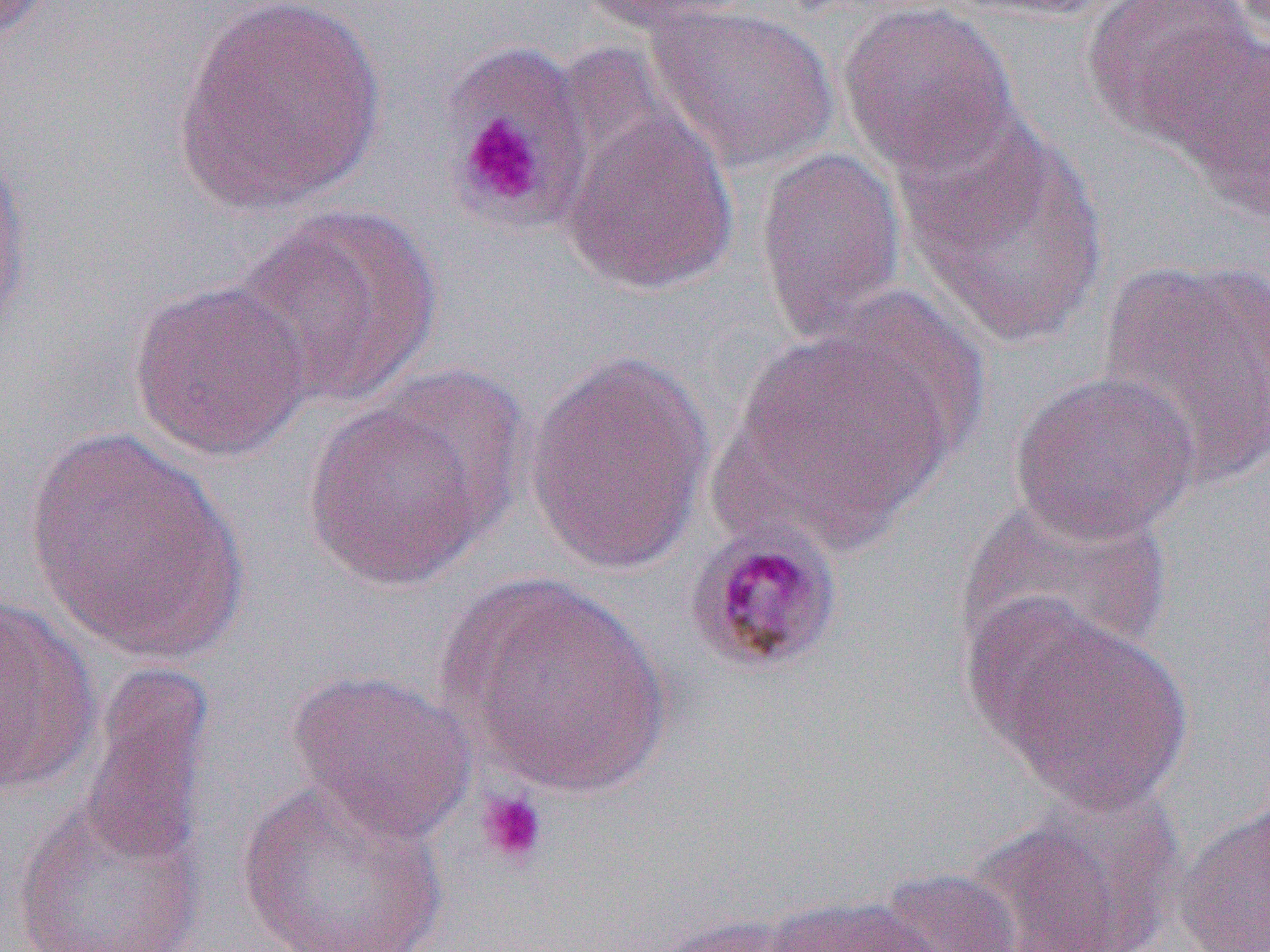
slide-level diagnosis = Plasmodium malariae
magnification = 1000x
uninfected red blood cell locations = approximate bounding boxes as (x1, y1, x2, y2) in pixels: (172, 0, 386, 216), (572, 0, 761, 34), (1082, 0, 1261, 144), (836, 2, 1019, 178), (646, 4, 839, 174), (1167, 33, 1268, 216), (444, 53, 584, 225), (557, 98, 741, 297), (895, 114, 1110, 348), (0, 143, 34, 344), (754, 146, 907, 344), (234, 206, 442, 410), (1092, 256, 1270, 489), (128, 279, 315, 463), (723, 331, 957, 548), (523, 348, 716, 575), (1009, 371, 1201, 544), (303, 395, 503, 591), (23, 427, 249, 668), (957, 494, 1173, 667), (446, 573, 672, 797), (0, 596, 100, 796), (976, 601, 1194, 814), (80, 661, 217, 872), (285, 668, 476, 845), (236, 776, 447, 952), (974, 796, 1180, 952), (11, 797, 206, 952), (1172, 800, 1270, 952), (875, 867, 1029, 952), (760, 894, 943, 951), (642, 912, 815, 952)
image size = 1270×952 pixels
field of view = one of a larger specimen
platelet locations = approximate bounding boxes as (x1, y1, x2, y2) in pixels: (444, 45, 590, 223), (455, 108, 550, 214), (475, 788, 548, 868)
modality = optical microscopy
preparation = thin blood film
Plasmodium malariae-infected red blood cell locations = approximate bounding boxes as (x1, y1, x2, y2) in pixels: (683, 520, 846, 678)